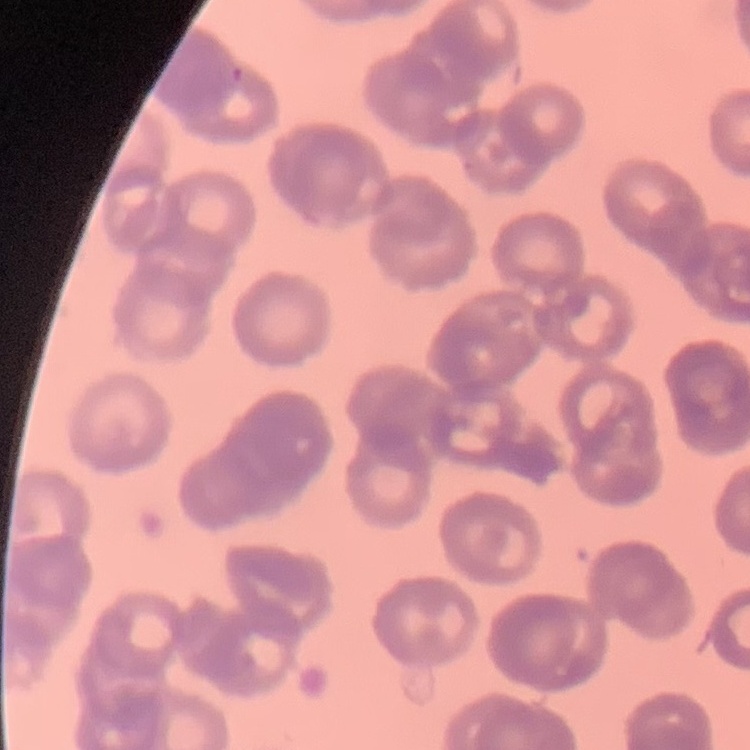
erythrocyte_morphology: rouleaux formation
preparation: thin peripheral smear
image_type: one tile cut from a larger photomicrograph
stain: Field's or Giemsa